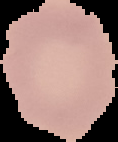
image_type: segmented cell region with the area outside set to black
preparation: thin blood film
image_size: 118×142 pixels
result: no Plasmodium parasites detected